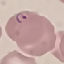

result: malaria parasites detected
stain: Giemsa
preparation: thin blood smear
capture: smartphone through the microscope eyepiece
image_type: cell patch, automatically extracted from a larger field of view and resized to 64 × 64 pixels